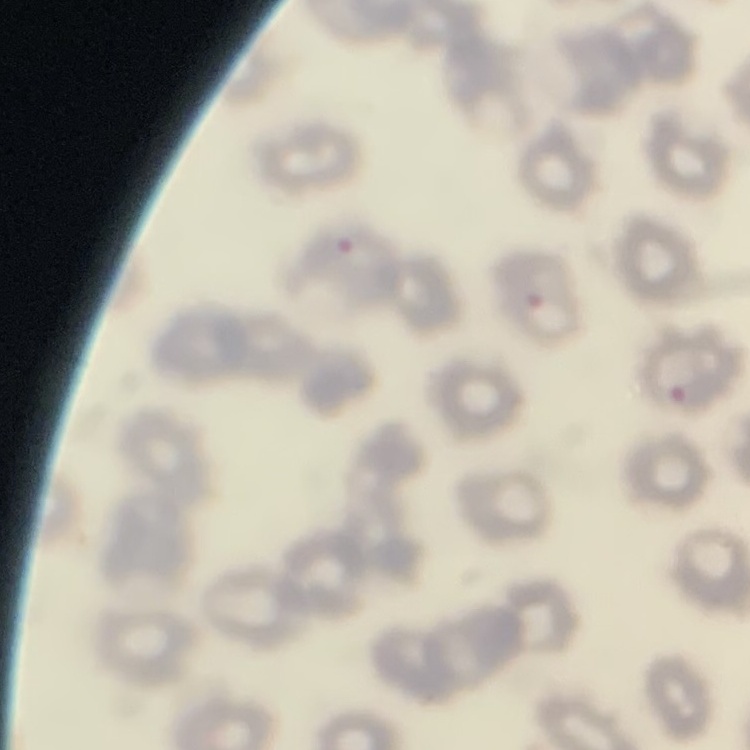

red blood cell morphology = no rouleaux formation
image type = square crop of a larger photomicrograph
preparation = thin blood smear
stain = Field's or Giemsa